Outline each Trypanosoma brucei.
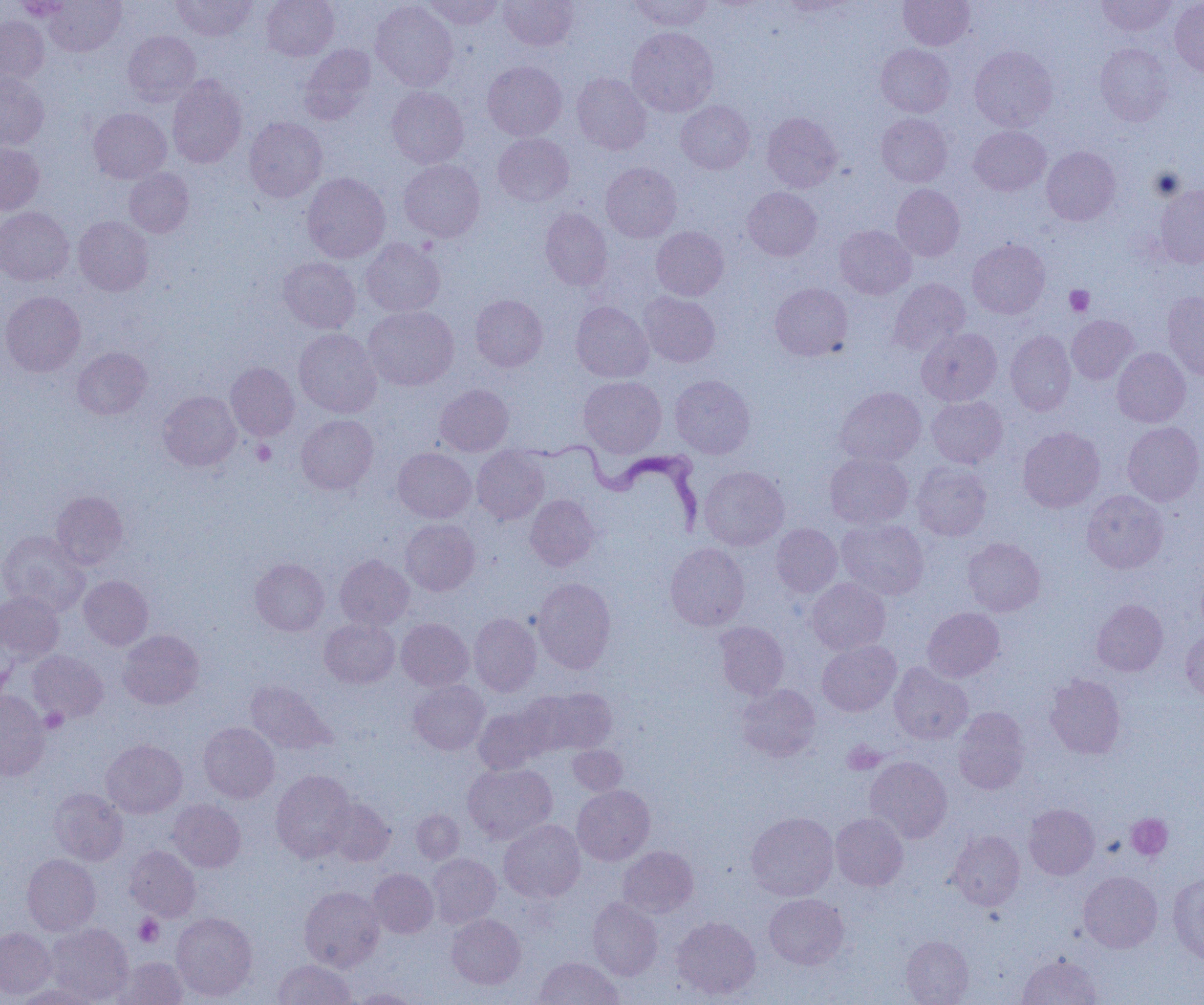

Approximate bounding boxes as named x1/y1/x2/y2 corners in pixels.
Trypanosoma brucei: (x1=519, y1=431, x2=706, y2=536).

slide-level diagnosis = Trypanosoma brucei
modality = optical microscopy
image size = 1204×1005 pixels
platelet locations = approximate bounding boxes as named x1/y1/x2/y2 corners in pixels: (x1=1065, y1=285, x2=1095, y2=316), (x1=251, y1=439, x2=276, y2=465), (x1=41, y1=708, x2=68, y2=733), (x1=842, y1=740, x2=886, y2=774), (x1=1126, y1=813, x2=1173, y2=860), (x1=134, y1=914, x2=164, y2=947)
field of view = one of a larger specimen
uninfected red blood cell locations = approximate bounding boxes as named x1/y1/x2/y2 corners in pixels: (x1=13, y1=0, x2=74, y2=20), (x1=44, y1=0, x2=125, y2=55), (x1=170, y1=0, x2=257, y2=41), (x1=261, y1=0, x2=339, y2=60), (x1=422, y1=0, x2=504, y2=30), (x1=628, y1=0, x2=714, y2=31), (x1=899, y1=0, x2=975, y2=50), (x1=1096, y1=0, x2=1177, y2=36), (x1=371, y1=1, x2=457, y2=91), (x1=499, y1=1, x2=577, y2=50), (x1=775, y1=1, x2=854, y2=15), (x1=1170, y1=1, x2=1204, y2=79), (x1=0, y1=15, x2=49, y2=87), (x1=627, y1=27, x2=718, y2=116), (x1=123, y1=30, x2=200, y2=105), (x1=876, y1=43, x2=955, y2=117), (x1=1095, y1=43, x2=1173, y2=126), (x1=299, y1=44, x2=376, y2=124), (x1=970, y1=46, x2=1057, y2=132), (x1=483, y1=61, x2=567, y2=140), (x1=0, y1=72, x2=49, y2=151), (x1=572, y1=73, x2=651, y2=154), (x1=167, y1=75, x2=246, y2=168), (x1=386, y1=86, x2=469, y2=168), (x1=676, y1=100, x2=754, y2=174), (x1=89, y1=107, x2=171, y2=183), (x1=762, y1=112, x2=842, y2=192), (x1=876, y1=113, x2=952, y2=187), (x1=244, y1=117, x2=327, y2=202), (x1=969, y1=126, x2=1051, y2=195), (x1=493, y1=133, x2=574, y2=207), (x1=0, y1=141, x2=45, y2=215), (x1=1042, y1=147, x2=1121, y2=225), (x1=398, y1=159, x2=485, y2=242), (x1=601, y1=162, x2=681, y2=241), (x1=124, y1=167, x2=194, y2=237), (x1=301, y1=172, x2=390, y2=262), (x1=892, y1=184, x2=965, y2=260), (x1=1154, y1=184, x2=1204, y2=268), (x1=743, y1=187, x2=822, y2=261), (x1=0, y1=207, x2=74, y2=285), (x1=540, y1=208, x2=612, y2=290), (x1=73, y1=215, x2=153, y2=296), (x1=834, y1=225, x2=916, y2=299), (x1=651, y1=226, x2=729, y2=300), (x1=361, y1=238, x2=445, y2=317), (x1=967, y1=239, x2=1050, y2=318), (x1=278, y1=257, x2=360, y2=333), (x1=889, y1=278, x2=970, y2=356), (x1=770, y1=283, x2=853, y2=361), (x1=0, y1=291, x2=85, y2=376), (x1=1162, y1=291, x2=1204, y2=380), (x1=639, y1=292, x2=720, y2=367), (x1=470, y1=295, x2=548, y2=372), (x1=571, y1=302, x2=653, y2=382), (x1=364, y1=306, x2=459, y2=390), (x1=1067, y1=315, x2=1138, y2=384), (x1=917, y1=328, x2=1002, y2=406), (x1=294, y1=329, x2=382, y2=417), (x1=1005, y1=330, x2=1076, y2=415), (x1=72, y1=347, x2=151, y2=419), (x1=1112, y1=348, x2=1190, y2=427), (x1=226, y1=362, x2=299, y2=440), (x1=670, y1=375, x2=755, y2=458), (x1=579, y1=376, x2=666, y2=458), (x1=435, y1=384, x2=513, y2=456), (x1=834, y1=386, x2=925, y2=467), (x1=158, y1=391, x2=241, y2=471), (x1=926, y1=396, x2=1008, y2=468), (x1=296, y1=415, x2=378, y2=494), (x1=1122, y1=422, x2=1204, y2=506), (x1=1018, y1=426, x2=1105, y2=512), (x1=472, y1=447, x2=550, y2=524), (x1=393, y1=448, x2=476, y2=522), (x1=825, y1=452, x2=913, y2=528), (x1=911, y1=461, x2=992, y2=541), (x1=699, y1=466, x2=788, y2=550), (x1=1082, y1=490, x2=1168, y2=573), (x1=51, y1=491, x2=127, y2=569), (x1=526, y1=494, x2=599, y2=571), (x1=401, y1=518, x2=480, y2=595), (x1=836, y1=518, x2=929, y2=599), (x1=770, y1=524, x2=842, y2=597), (x1=0, y1=531, x2=90, y2=617), (x1=962, y1=537, x2=1045, y2=617), (x1=665, y1=543, x2=749, y2=630), (x1=335, y1=555, x2=414, y2=630), (x1=250, y1=559, x2=329, y2=636), (x1=79, y1=575, x2=153, y2=650), (x1=533, y1=577, x2=616, y2=673), (x1=806, y1=578, x2=891, y2=654), (x1=0, y1=591, x2=63, y2=662), (x1=1091, y1=599, x2=1168, y2=676), (x1=922, y1=607, x2=1004, y2=682), (x1=469, y1=613, x2=541, y2=696), (x1=319, y1=617, x2=400, y2=688), (x1=396, y1=618, x2=473, y2=691), (x1=715, y1=622, x2=789, y2=699), (x1=118, y1=629, x2=203, y2=709), (x1=1181, y1=629, x2=1204, y2=702), (x1=817, y1=640, x2=901, y2=716), (x1=27, y1=650, x2=108, y2=723), (x1=889, y1=662, x2=972, y2=745), (x1=1045, y1=674, x2=1125, y2=758), (x1=245, y1=680, x2=334, y2=754), (x1=409, y1=680, x2=489, y2=755), (x1=737, y1=684, x2=820, y2=761), (x1=531, y1=687, x2=618, y2=754), (x1=0, y1=691, x2=50, y2=779), (x1=473, y1=705, x2=552, y2=774), (x1=953, y1=707, x2=1031, y2=794), (x1=199, y1=722, x2=279, y2=803), (x1=101, y1=739, x2=187, y2=818), (x1=568, y1=745, x2=627, y2=795), (x1=864, y1=756, x2=952, y2=843), (x1=463, y1=762, x2=557, y2=843), (x1=271, y1=770, x2=355, y2=862), (x1=573, y1=785, x2=655, y2=865), (x1=49, y1=788, x2=127, y2=865), (x1=325, y1=798, x2=395, y2=866), (x1=168, y1=799, x2=246, y2=872), (x1=1024, y1=804, x2=1099, y2=879), (x1=411, y1=809, x2=464, y2=864), (x1=746, y1=811, x2=838, y2=900), (x1=831, y1=812, x2=908, y2=891), (x1=499, y1=819, x2=585, y2=903), (x1=948, y1=831, x2=1025, y2=910), (x1=124, y1=845, x2=201, y2=921), (x1=618, y1=846, x2=698, y2=918), (x1=22, y1=854, x2=101, y2=935), (x1=428, y1=854, x2=501, y2=928), (x1=368, y1=868, x2=438, y2=938), (x1=1079, y1=871, x2=1162, y2=953), (x1=1168, y1=872, x2=1204, y2=965), (x1=299, y1=886, x2=384, y2=972), (x1=764, y1=893, x2=848, y2=969), (x1=587, y1=897, x2=663, y2=980), (x1=171, y1=912, x2=257, y2=1001), (x1=447, y1=914, x2=526, y2=988), (x1=672, y1=916, x2=760, y2=999), (x1=44, y1=923, x2=133, y2=1004), (x1=0, y1=927, x2=56, y2=1000), (x1=901, y1=935, x2=974, y2=1004), (x1=1018, y1=954, x2=1103, y2=1005), (x1=111, y1=956, x2=188, y2=1004), (x1=535, y1=957, x2=623, y2=1005), (x1=273, y1=959, x2=355, y2=1005), (x1=13, y1=984, x2=102, y2=1005), (x1=350, y1=988, x2=423, y2=1004)
preparation = thin blood film
magnification = 1000x